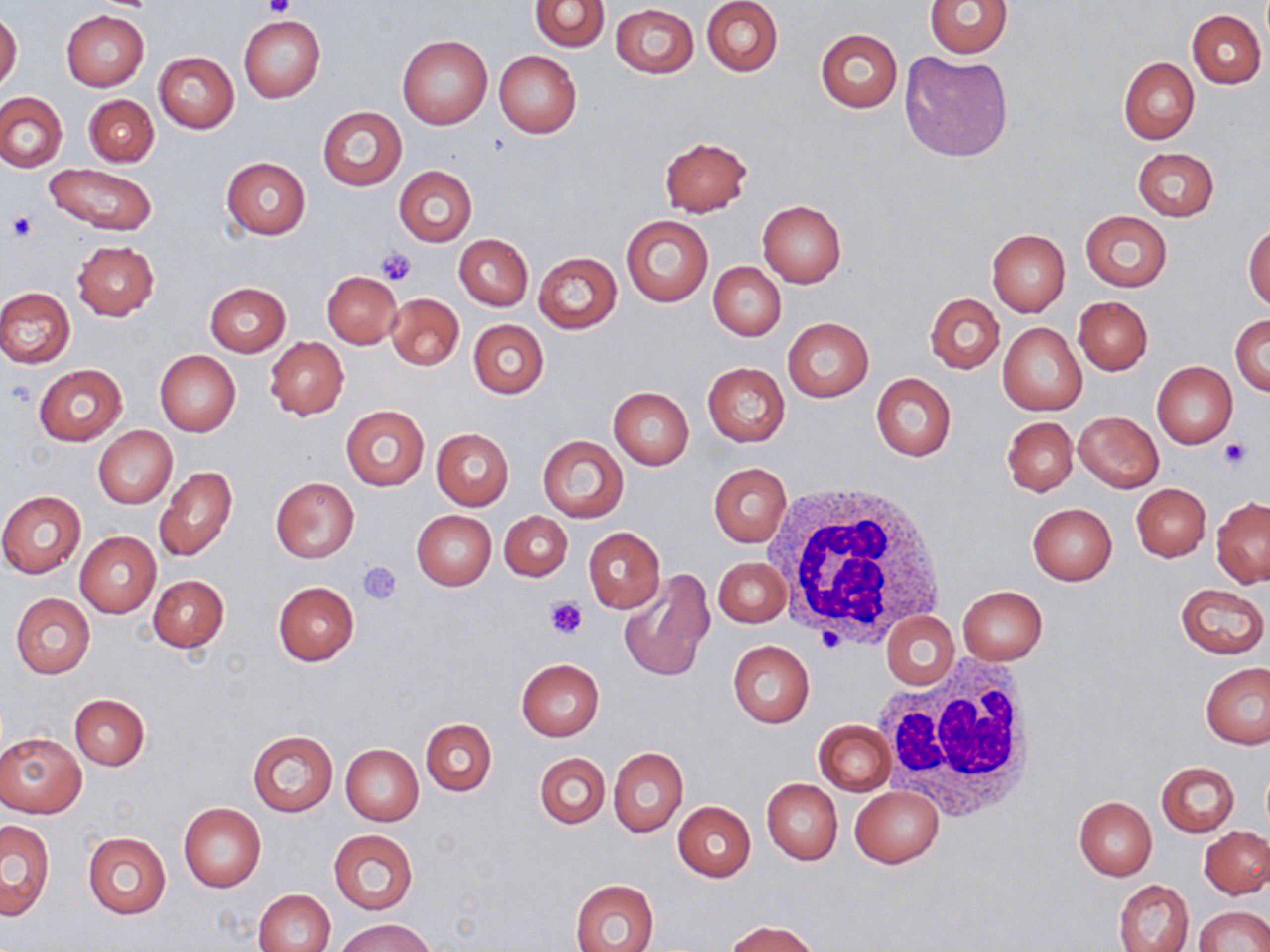
Summary:
  - Coordinate format: approximate bounding boxes as [x1, y1, x2, y2] in pixels
  - Platelet locations: [265, 0, 294, 20], [6, 211, 38, 241], [375, 246, 418, 287], [6, 380, 34, 407], [1219, 439, 1251, 469], [356, 560, 403, 605], [546, 595, 589, 640]
  - Uninfected red blood cell locations: [530, 0, 609, 52], [701, 0, 782, 77], [924, 0, 1014, 59], [610, 4, 698, 79], [1188, 10, 1266, 89], [61, 11, 149, 92], [0, 13, 22, 92], [239, 16, 325, 103], [815, 27, 903, 112], [398, 34, 492, 130], [494, 50, 582, 137], [154, 51, 238, 132], [899, 51, 1013, 162], [1118, 57, 1199, 143], [0, 92, 67, 171], [84, 95, 159, 168], [316, 106, 407, 192], [658, 137, 753, 217], [1132, 148, 1220, 221], [220, 156, 311, 239], [45, 162, 158, 235], [393, 166, 477, 248], [757, 200, 846, 287], [1080, 211, 1172, 291], [621, 214, 713, 307], [1243, 221, 1270, 310], [987, 229, 1070, 316], [454, 234, 533, 311], [72, 241, 160, 321], [533, 251, 621, 334], [709, 261, 786, 341], [322, 272, 402, 348], [204, 283, 292, 356], [0, 287, 75, 368], [385, 293, 464, 371], [925, 293, 1004, 374], [1074, 296, 1152, 375], [1231, 314, 1269, 396], [783, 317, 874, 402], [468, 319, 549, 399], [998, 322, 1087, 415], [266, 338, 349, 420], [155, 350, 241, 436], [703, 362, 790, 447], [1153, 362, 1237, 449], [33, 365, 127, 446], [871, 374, 956, 461], [608, 386, 694, 469], [341, 405, 429, 490], [1074, 411, 1164, 491], [1003, 417, 1078, 496], [93, 426, 177, 508], [431, 428, 513, 510], [537, 436, 628, 521], [709, 463, 792, 547], [155, 465, 238, 562], [271, 478, 358, 562], [1132, 484, 1210, 562], [0, 491, 87, 578], [1211, 498, 1270, 588], [1027, 503, 1117, 585], [411, 510, 496, 590], [500, 511, 572, 581], [584, 529, 665, 612], [76, 531, 160, 617], [713, 556, 790, 628], [617, 567, 716, 682], [149, 575, 229, 652], [272, 582, 359, 666], [1176, 583, 1269, 659], [958, 587, 1048, 664], [10, 594, 94, 680], [882, 612, 959, 690], [728, 640, 814, 728], [516, 659, 605, 740], [1201, 661, 1270, 749], [69, 694, 149, 770], [421, 719, 496, 796], [813, 720, 895, 795], [247, 729, 337, 817], [0, 731, 87, 818], [340, 744, 424, 825], [608, 748, 687, 836], [535, 752, 610, 829], [1156, 761, 1240, 836], [762, 779, 841, 864], [850, 786, 944, 868], [1074, 796, 1157, 880], [672, 800, 756, 881], [178, 803, 266, 892], [0, 820, 55, 919], [1200, 826, 1270, 898], [329, 830, 418, 915], [82, 833, 171, 919], [571, 879, 658, 952], [1114, 880, 1193, 952], [254, 889, 335, 952], [1195, 905, 1270, 952], [337, 919, 434, 952], [724, 920, 821, 952]
  - White blood cell locations: [770, 485, 948, 655], [875, 656, 1042, 823]
  - Slide-level diagnosis: negative for blood parasites
  - Modality: light microscopy
  - Magnification: 1000x
  - Stain: May-Grünwald-Giemsa
  - Image size: 1270×952 pixels
  - Preparation: thin blood smear
  - Field of view: one of a larger specimen